Report the malaria status.
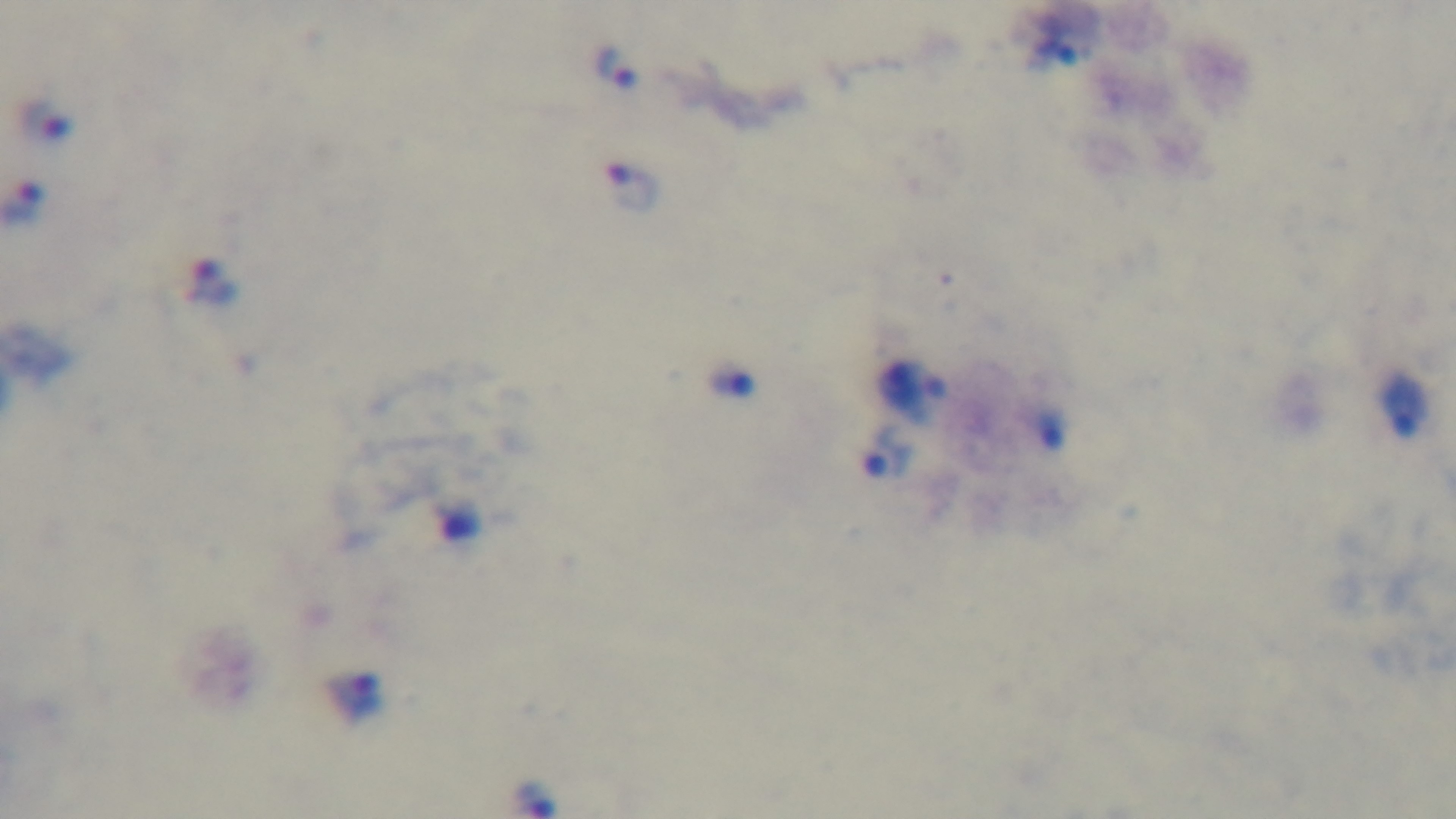
Infected.

Photomicrograph. Captured with a mounted 4K digital camera. One field from the slide. 100x oil-immersion objective. Preparation: thick blood film. Giemsa stain.